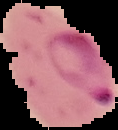 Malaria status: parasitized. From a thin blood smear. Cell region segmented out of the field of view; the surrounding area is masked to black. Image is 118×130 pixels.